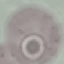

{
  "result": "no malaria parasites seen",
  "preparation": "thin blood smear",
  "capture": "smartphone camera at the microscope eyepiece",
  "image_type": "cell patch, automatically extracted from a larger field of view and resized to 64 × 64 pixels",
  "stain": "Giemsa"
}